Identify the preparation type.
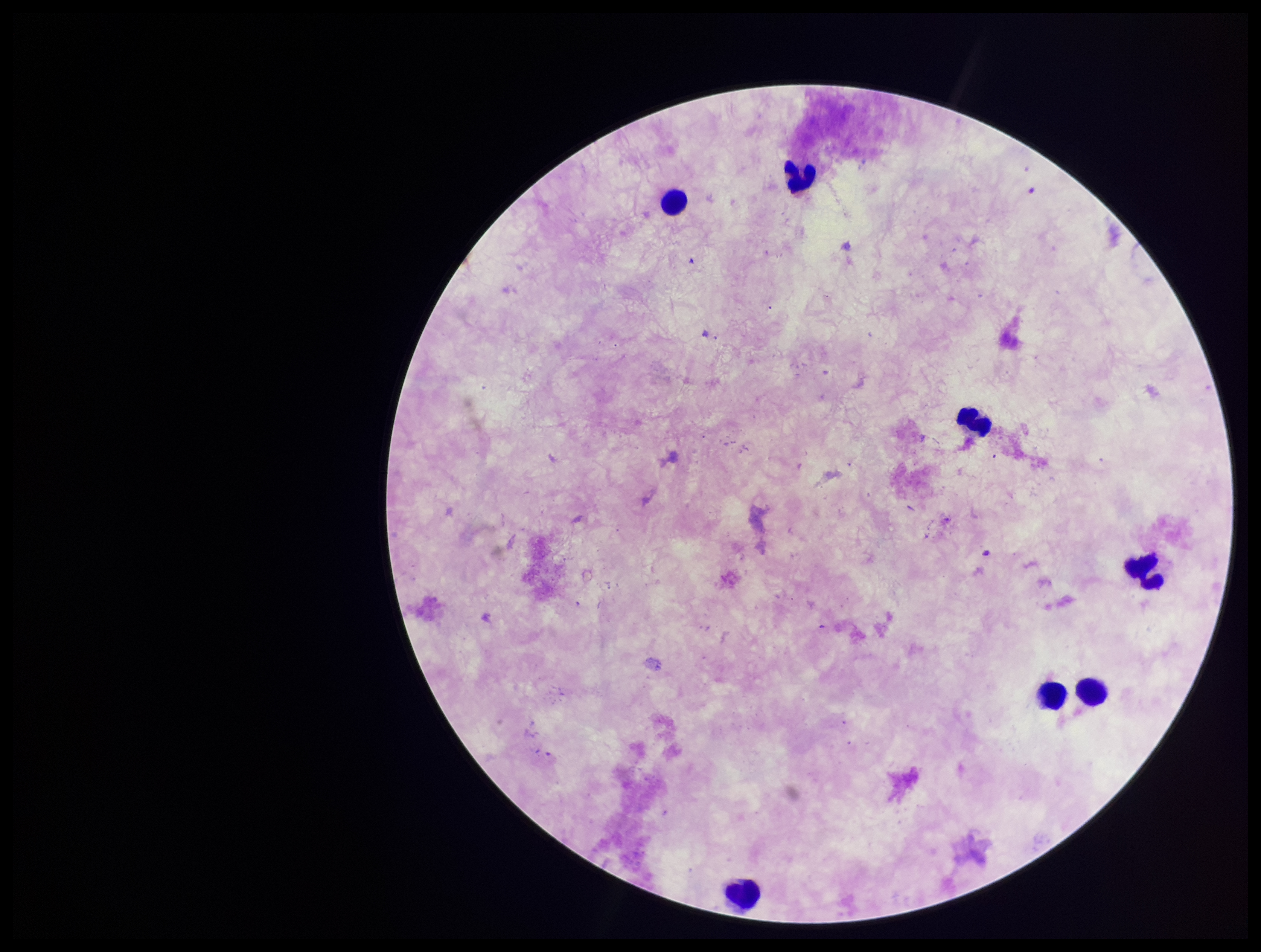
Thick.

Leukocyte count: 7. Single field of view. Patient malaria status: negative. Parasite count: 0. Image is 1261×952 pixels. Smartphone photograph taken through the eyepiece of a microscope. Giemsa stain. Plasmodium parasites: none identified.